Assess this cell for malaria.
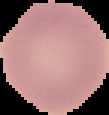

It is uninfected.

preparation = thin blood smear
image type = segmented cell region on a black background
image size = 109×115 pixels